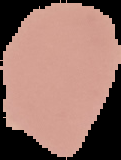
Malaria status: uninfected. Image is 121×160 pixels. From a thin blood smear. Cell region segmented out of the field of view; the surrounding area is masked to black.